Identify the blood parasite species.
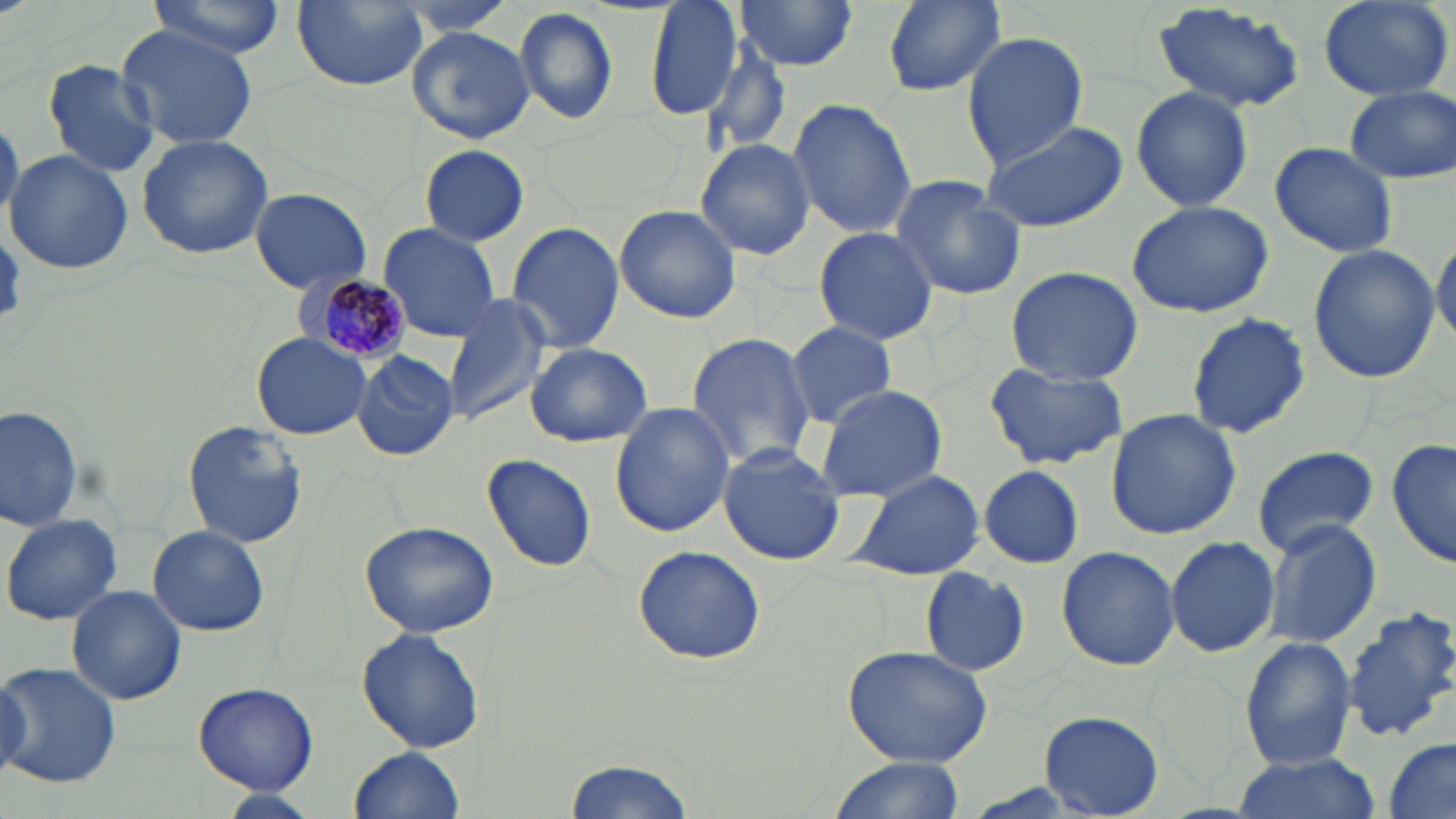

Plasmodium malariae.

Approximate bounding boxes as (x1, y1, x2, y2) in pixels. Plasmodium malariae-infected red blood cell locations: (287, 274, 411, 367). Uninfected red blood cell locations: (144, 0, 287, 61), (290, 0, 430, 92), (388, 0, 525, 35), (644, 0, 745, 119), (733, 0, 860, 75), (876, 0, 1008, 96), (1317, 0, 1454, 103), (1154, 2, 1310, 113), (512, 6, 620, 127), (116, 24, 261, 152), (405, 25, 535, 146), (960, 30, 1088, 169), (696, 37, 794, 166), (42, 60, 161, 178), (1344, 85, 1454, 184), (1130, 86, 1254, 211), (786, 96, 917, 241), (0, 114, 21, 228), (978, 118, 1128, 234), (136, 133, 273, 260), (695, 139, 815, 260), (1269, 140, 1398, 259), (419, 144, 531, 247), (5, 150, 134, 275), (888, 175, 1026, 301), (249, 186, 371, 293), (1125, 199, 1275, 318), (614, 205, 742, 323), (506, 222, 625, 355), (377, 224, 502, 342), (812, 226, 939, 346), (1432, 232, 1456, 347), (1307, 244, 1439, 385), (1003, 266, 1143, 387), (440, 295, 550, 426), (1189, 312, 1311, 439), (786, 320, 897, 428), (252, 331, 371, 439), (685, 332, 817, 470), (524, 343, 653, 448), (352, 351, 461, 460), (984, 364, 1128, 471), (812, 386, 948, 502), (609, 402, 736, 539), (1, 406, 85, 532), (1104, 408, 1242, 540), (183, 421, 306, 549), (1388, 439, 1454, 571), (717, 444, 847, 566), (1249, 444, 1380, 557), (481, 452, 598, 572), (974, 464, 1088, 568), (846, 468, 987, 582), (3, 512, 125, 626), (1262, 518, 1383, 649), (359, 519, 501, 639), (148, 525, 268, 636), (1166, 535, 1280, 658), (632, 544, 766, 665), (1057, 545, 1179, 671), (919, 566, 1032, 676), (67, 585, 186, 705), (1343, 607, 1456, 737), (356, 627, 486, 755), (1240, 637, 1357, 770), (842, 644, 993, 767), (1, 659, 122, 791), (190, 682, 322, 794), (1039, 710, 1163, 816), (1382, 737, 1456, 818), (350, 746, 465, 819), (1228, 752, 1382, 819), (565, 755, 698, 819), (825, 755, 964, 819), (215, 790, 323, 819). 1000x magnification. May-Grünwald-Giemsa stain. Image is 1456×819 pixels. Single field of view. Light microscopy. Thin blood smear.